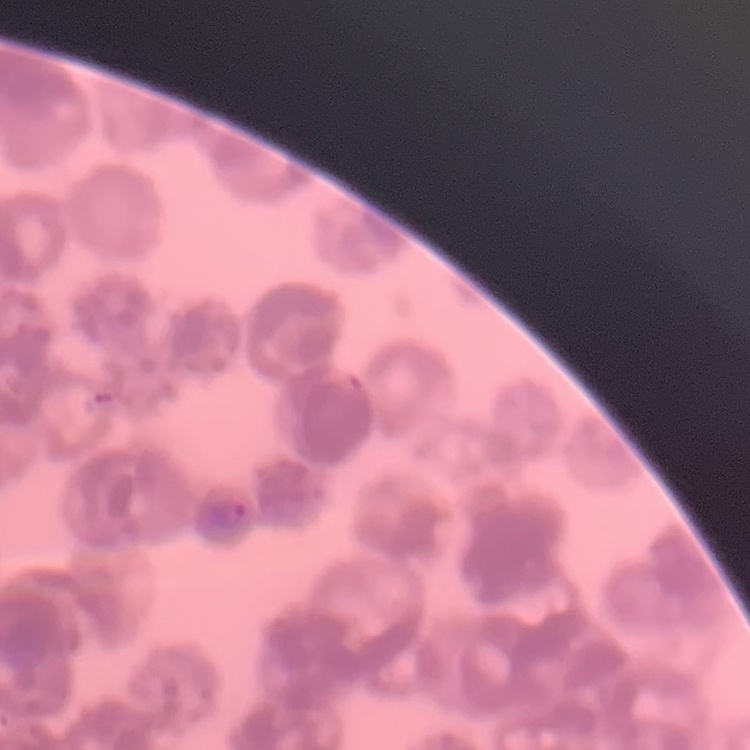
Summary:
  - Red blood cell morphology: rouleaux formation
  - Stain: Field's or Giemsa
  - Preparation: thin blood smear
  - Image type: one tile cut from a larger photomicrograph